State the blood parasite species.
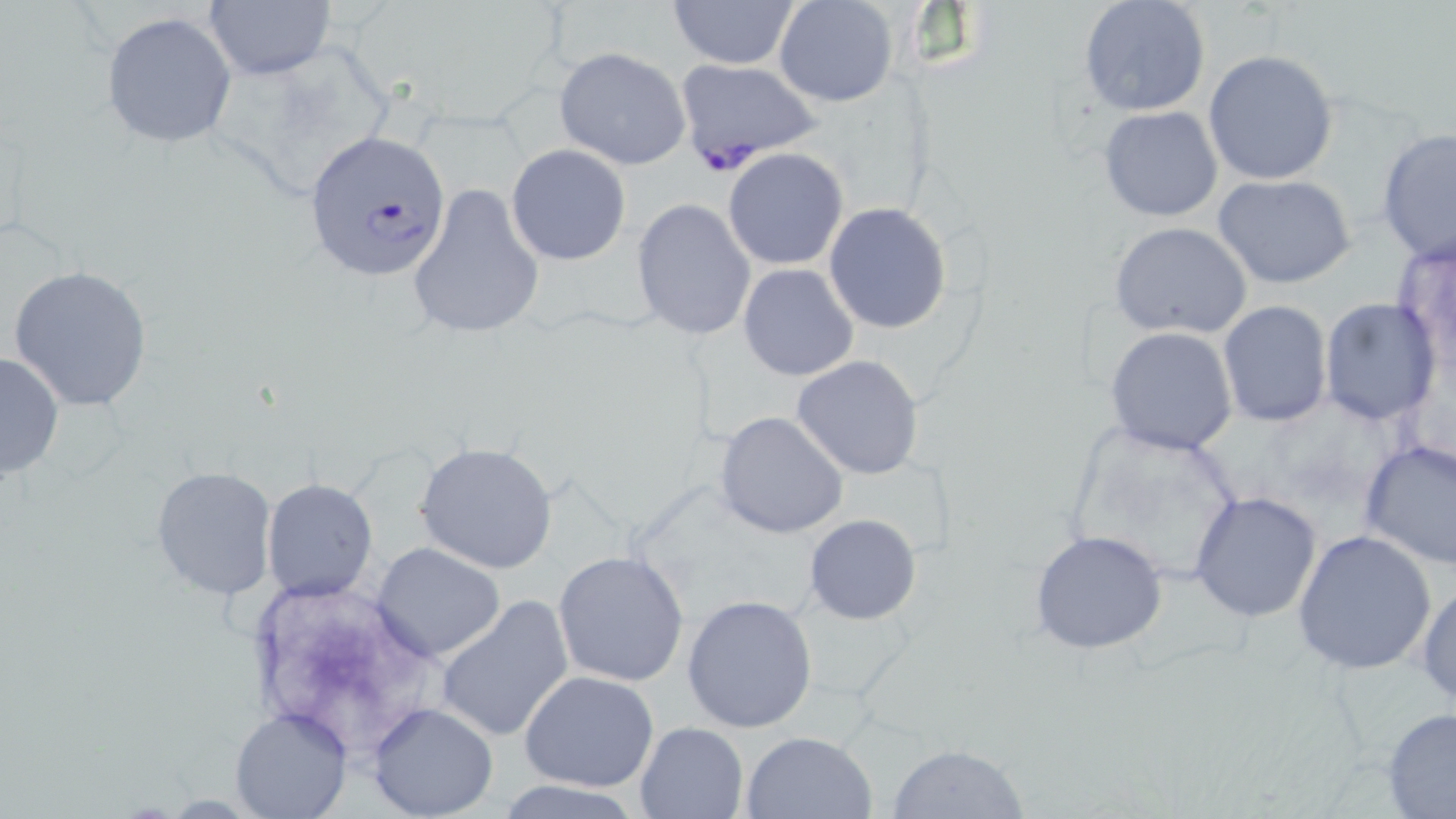

Plasmodium falciparum.

Summary:
  - Coordinate format: approximate bounding boxes as [x1, y1, x2, y2] in pixels
  - Uninfected red blood cell locations: [668, 0, 801, 70], [774, 0, 896, 107], [1079, 0, 1211, 118], [203, 1, 336, 80], [101, 12, 238, 148], [555, 47, 691, 169], [1203, 49, 1339, 186], [1098, 105, 1224, 223], [1376, 129, 1456, 266], [506, 144, 631, 267], [723, 148, 849, 270], [1211, 174, 1358, 290], [407, 182, 547, 342], [632, 198, 756, 342], [824, 202, 952, 334], [1109, 221, 1253, 340], [1393, 235, 1456, 375], [737, 264, 859, 382], [7, 266, 155, 412], [1319, 297, 1441, 426], [1218, 299, 1332, 428], [1104, 326, 1239, 454], [0, 350, 64, 481], [792, 355, 925, 479], [716, 411, 848, 539], [1358, 437, 1456, 570], [414, 442, 558, 574], [150, 465, 277, 599], [262, 479, 379, 603], [1190, 491, 1322, 622], [804, 513, 920, 624], [1028, 529, 1170, 655], [1291, 529, 1438, 676], [372, 542, 507, 662], [553, 551, 692, 688], [1417, 576, 1456, 709], [682, 594, 818, 734], [434, 596, 575, 742], [520, 669, 660, 792], [367, 702, 498, 819], [230, 707, 351, 819], [1381, 707, 1456, 817], [634, 721, 747, 818], [740, 730, 876, 819], [886, 744, 1030, 818], [496, 779, 643, 818]
  - Plasmodium falciparum-infected red blood cell locations: [674, 58, 823, 170], [302, 132, 451, 281]
  - Image size: 1456×819 pixels
  - Magnification: 1000x
  - Field of view: single
  - Modality: optical microscopy
  - Preparation: thin blood film
  - Stain: May-Grünwald-Giemsa